Classify this cell by malaria status.
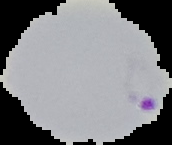
It is parasitized.

From a thin blood smear. The area outside the segmented cell region is set to black. Image is 172×145 pixels.